State which cell type is depicted.
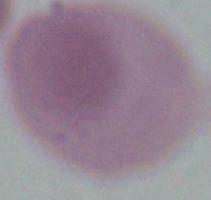
This is an erythrocyte.

Captured at 1000x magnification. Micrograph.